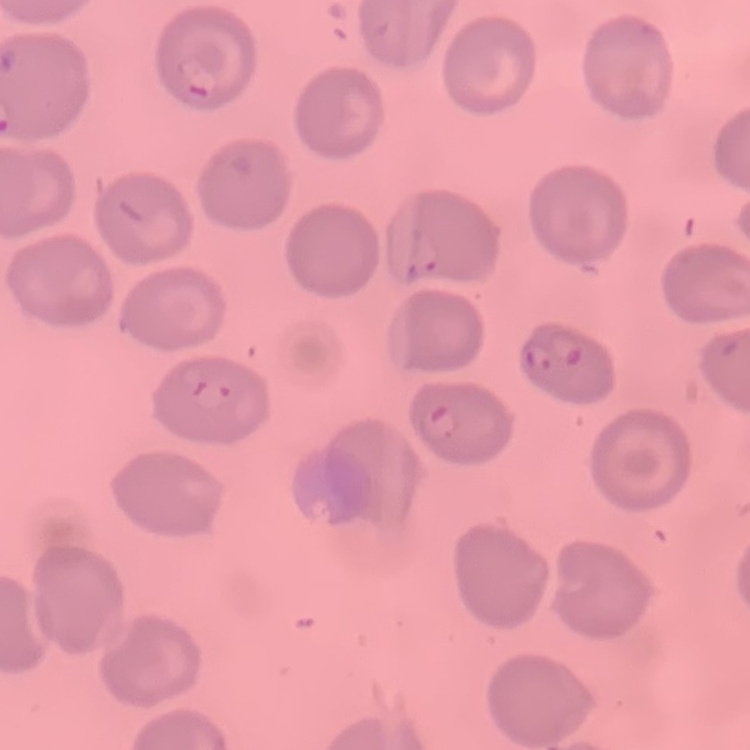

red blood cell morphology = no rouleaux formation
stain = Field's or Giemsa
image type = square crop of a larger photomicrograph
preparation = thin peripheral smear